Look for Plasmodium parasites.
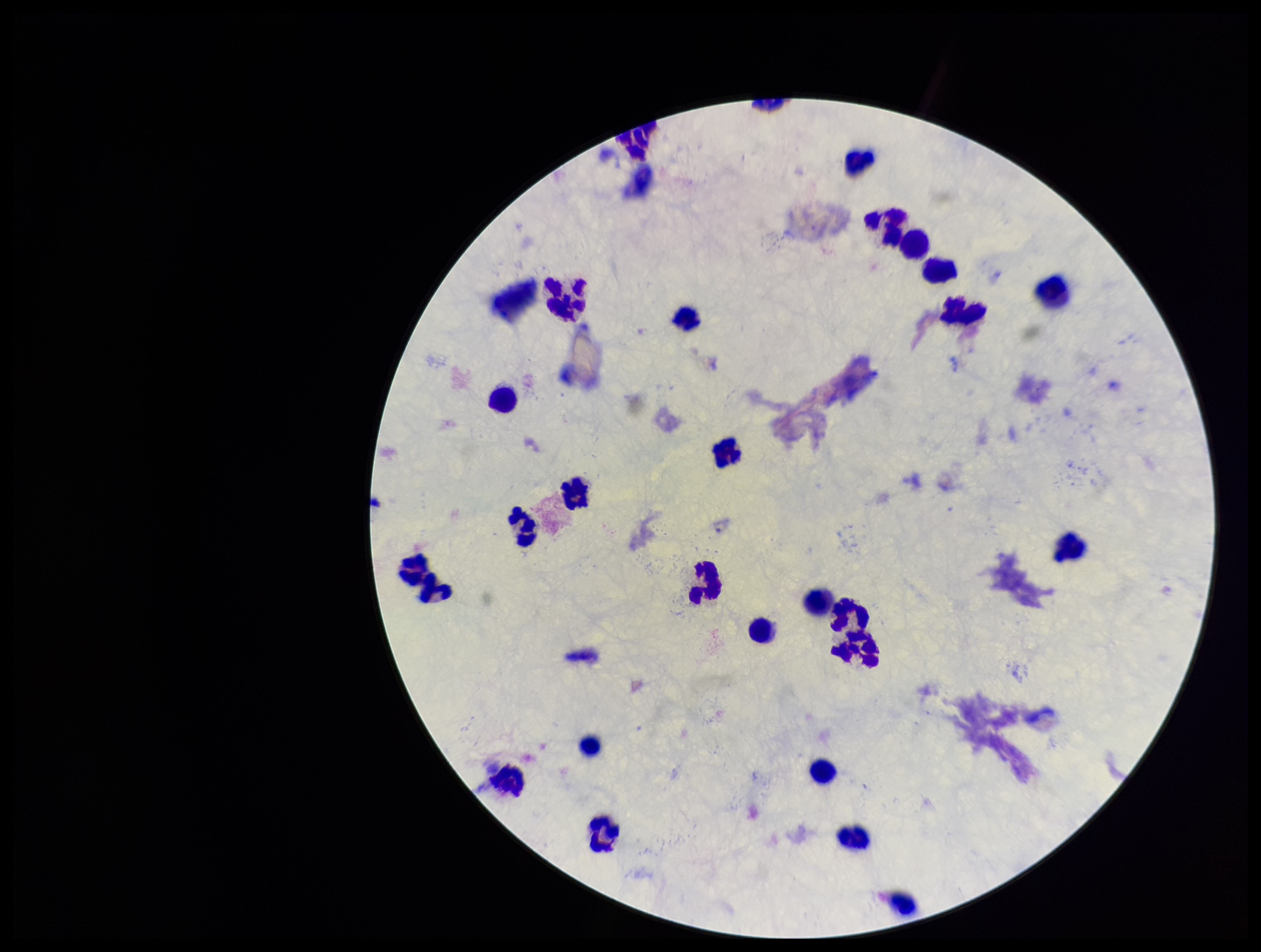
None seen.

Summary:
  - Preparation: thick
  - Parasite count: 0
  - Stain: Giemsa
  - Leukocyte count: 29
  - Field of view: single
  - Patient malaria status: negative
  - Capture: smartphone photograph through the microscope eyepiece
  - Image size: 1261×952 pixels